Locate every blood parasite and identify its species.
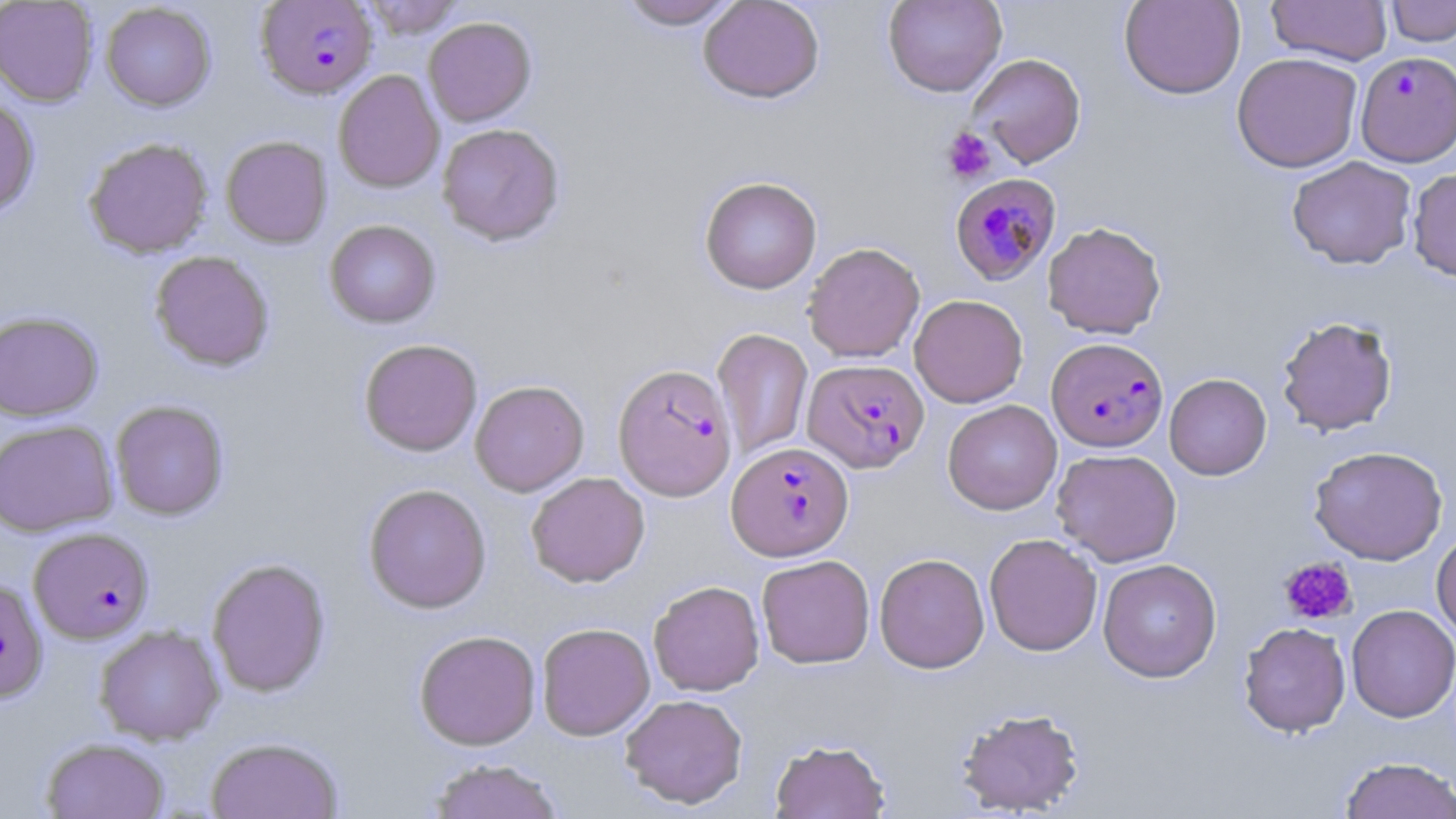

Approximate bounding boxes as named x1/y1/x2/y2 corners in pixels.
Plasmodium falciparum-infected red blood cells: (x1=256, y1=1, x2=378, y2=99), (x1=1355, y1=51, x2=1456, y2=168), (x1=949, y1=172, x2=1062, y2=285), (x1=1046, y1=337, x2=1168, y2=452), (x1=802, y1=358, x2=930, y2=474), (x1=613, y1=363, x2=737, y2=501), (x1=727, y1=441, x2=853, y2=561), (x1=29, y1=527, x2=154, y2=644), (x1=0, y1=577, x2=48, y2=702).
No Plasmodium ovale, Plasmodium malariae, Plasmodium vivax, Babesia divergens, or Trypanosoma brucei observed.

Uninfected red blood cell locations: (x1=0, y1=0, x2=99, y2=107), (x1=360, y1=0, x2=464, y2=39), (x1=615, y1=0, x2=742, y2=30), (x1=698, y1=0, x2=824, y2=103), (x1=882, y1=0, x2=1007, y2=97), (x1=1119, y1=0, x2=1245, y2=99), (x1=1386, y1=0, x2=1455, y2=46), (x1=1267, y1=1, x2=1392, y2=65), (x1=101, y1=3, x2=216, y2=111), (x1=423, y1=17, x2=537, y2=126), (x1=1232, y1=52, x2=1363, y2=173), (x1=968, y1=53, x2=1086, y2=168), (x1=333, y1=70, x2=444, y2=192), (x1=0, y1=96, x2=40, y2=217), (x1=437, y1=123, x2=565, y2=245), (x1=220, y1=135, x2=332, y2=249), (x1=83, y1=136, x2=213, y2=258), (x1=1286, y1=156, x2=1417, y2=270), (x1=1407, y1=168, x2=1456, y2=282), (x1=699, y1=175, x2=822, y2=294), (x1=324, y1=220, x2=440, y2=328), (x1=1043, y1=221, x2=1167, y2=339), (x1=802, y1=242, x2=925, y2=363), (x1=149, y1=250, x2=274, y2=372), (x1=909, y1=294, x2=1028, y2=408), (x1=0, y1=310, x2=103, y2=422), (x1=1276, y1=315, x2=1399, y2=436), (x1=712, y1=327, x2=813, y2=461), (x1=359, y1=338, x2=483, y2=456), (x1=1164, y1=373, x2=1272, y2=480), (x1=470, y1=380, x2=589, y2=496), (x1=110, y1=399, x2=229, y2=520), (x1=943, y1=399, x2=1062, y2=515), (x1=0, y1=419, x2=119, y2=536), (x1=1308, y1=445, x2=1448, y2=565), (x1=1051, y1=448, x2=1182, y2=566), (x1=526, y1=472, x2=650, y2=587), (x1=363, y1=483, x2=492, y2=613), (x1=1431, y1=530, x2=1456, y2=642), (x1=984, y1=533, x2=1103, y2=656), (x1=874, y1=552, x2=990, y2=673), (x1=757, y1=555, x2=875, y2=668), (x1=206, y1=558, x2=331, y2=697), (x1=1098, y1=558, x2=1222, y2=682), (x1=648, y1=580, x2=764, y2=696), (x1=1346, y1=604, x2=1456, y2=722), (x1=1238, y1=621, x2=1351, y2=738), (x1=537, y1=622, x2=655, y2=740), (x1=94, y1=625, x2=225, y2=745), (x1=414, y1=629, x2=541, y2=750), (x1=620, y1=694, x2=748, y2=809), (x1=955, y1=707, x2=1086, y2=816), (x1=205, y1=736, x2=344, y2=819), (x1=40, y1=737, x2=170, y2=819), (x1=769, y1=739, x2=891, y2=818), (x1=1339, y1=756, x2=1456, y2=819), (x1=425, y1=759, x2=565, y2=819). Platelet locations: (x1=942, y1=127, x2=997, y2=184), (x1=1280, y1=557, x2=1357, y2=625). Slide-level diagnosis: Plasmodium falciparum. Thin blood film. Captured at 1000x magnification. May-Grünwald-Giemsa-stained preparation. Image is 1456×819 pixels. One field of a larger specimen. Light microscopy.